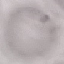
Summary:
  - Malaria status: uninfected
  - Stain: Giemsa
  - Image type: cell patch, automatically extracted from a larger field of view and resized to 64 × 64 pixels
  - Preparation: thin blood smear
  - Capture: smartphone through the microscope eyepiece